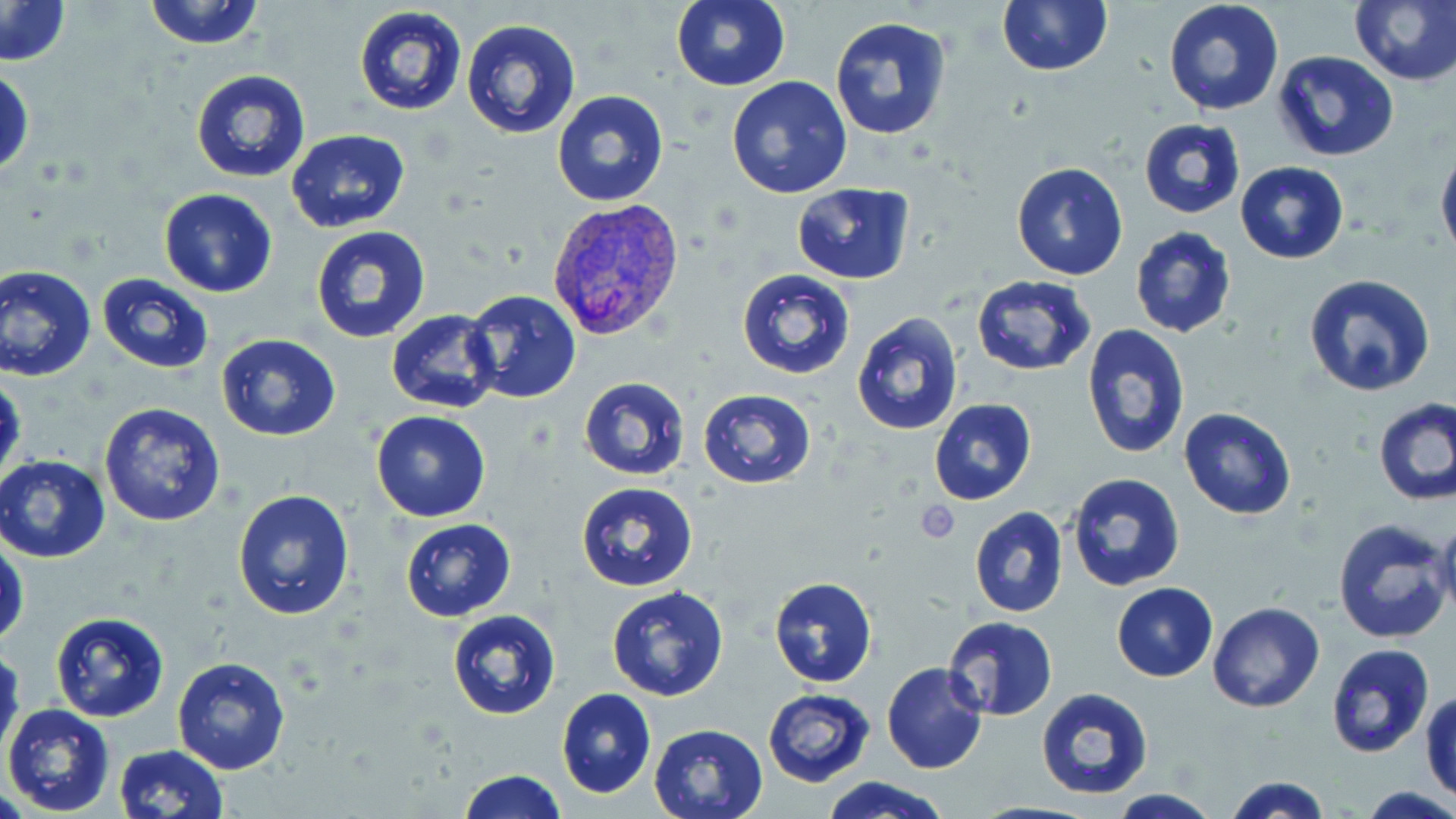

slide_level_diagnosis: Plasmodium vivax
field_of_view: single
plasmodium_vivax_infected_red_blood_cell_locations: 'approximate bounding boxes as (x1,y1)-(x2,y2) corner pairs in pixels: (545,197)-(684,343)'
uninfected_red_blood_cell_locations: 'approximate bounding boxes as (x1,y1)-(x2,y2) corner pairs in pixels: (142,0)-(266,50), (670,0)-(789,90), (996,0)-(1111,75), (1162,0)-(1287,116), (1,1)-(72,67), (1349,1)-(1456,85), (352,5)-(468,116), (829,14)-(956,141), (461,18)-(581,138), (1273,50)-(1398,162), (1,63)-(34,181), (190,69)-(311,184), (726,77)-(853,201), (552,89)-(668,206), (1138,118)-(1247,219), (286,129)-(413,235), (1436,147)-(1456,264), (1235,160)-(1349,264), (1011,162)-(1128,281), (791,182)-(915,284), (159,188)-(277,297), (1130,226)-(1237,339), (310,227)-(432,344), (1,264)-(97,382), (736,269)-(855,380), (1303,273)-(1437,397), (97,274)-(214,373), (971,275)-(1096,376), (463,289)-(581,404), (387,310)-(500,412), (852,311)-(964,436), (1081,325)-(1190,462), (217,335)-(341,440), (0,376)-(24,485), (579,376)-(691,481), (698,389)-(816,489), (1374,397)-(1455,507), (930,398)-(1036,505), (100,403)-(226,527), (1179,406)-(1297,521), (371,411)-(491,522), (0,454)-(113,563), (1065,472)-(1185,594), (577,481)-(698,592), (232,489)-(355,620), (969,505)-(1068,618), (1435,516)-(1456,618), (401,518)-(515,621), (1332,518)-(1453,645), (0,537)-(26,651), (769,577)-(877,687), (1113,583)-(1218,681), (606,585)-(728,700), (1209,603)-(1325,714), (446,610)-(561,722), (50,611)-(169,722), (941,617)-(1057,722), (1,638)-(22,762), (1324,643)-(1434,760), (172,656)-(290,774), (882,662)-(986,774), (1035,687)-(1155,802), (556,688)-(655,799), (763,688)-(874,785), (1421,691)-(1456,799), (2,704)-(116,817), (648,723)-(768,819), (114,744)-(227,818), (459,770)-(567,818), (822,776)-(949,819), (1224,777)-(1333,819), (1360,786)-(1456,819), (1104,792)-(1224,819)'
magnification: 1000x
preparation: thin blood smear
platelet_locations: 'approximate bounding boxes as (x1,y1)-(x2,y2) corner pairs in pixels: (918,499)-(962,542)'
modality: optical microscopy
image_size: 1456×819 pixels
stain: May-Grünwald-Giemsa